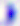
magnification = 400x
identification = Toxoplasma gondii
modality = photomicrograph